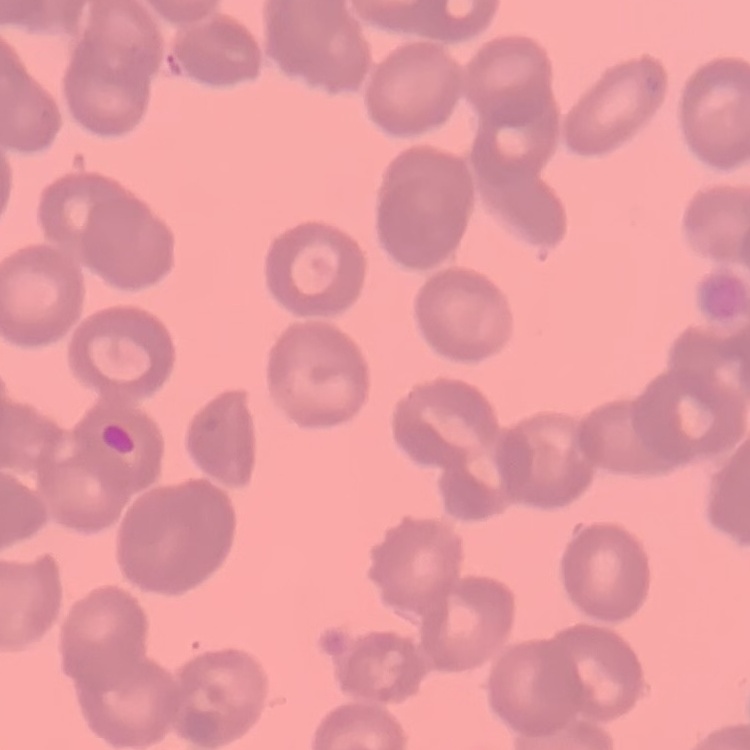
red_blood_cell_morphology: rouleaux formation
image_type: square crop of a larger photomicrograph
preparation: thin blood film
stain: Field's or Giemsa